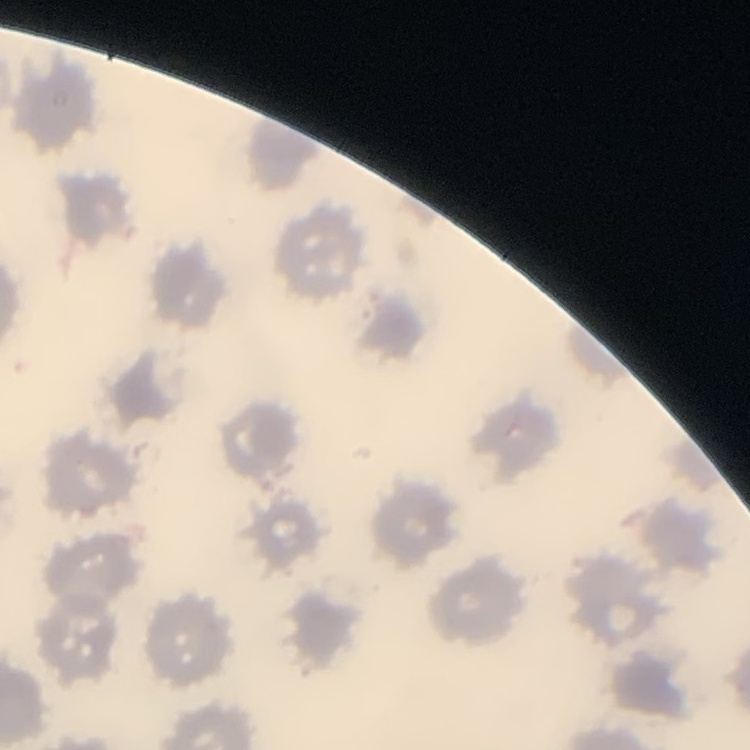 The red blood cells exhibit no rouleaux formation. One tile cut from a larger photomicrograph. Thin blood smear. Stained with either Field's or Giemsa.